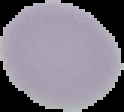
image size = 124×112 pixels
preparation = thin blood smear
result = no Plasmodium parasites seen
image type = segmented cell region on a black background